Comment on the morphology of the red blood cells.
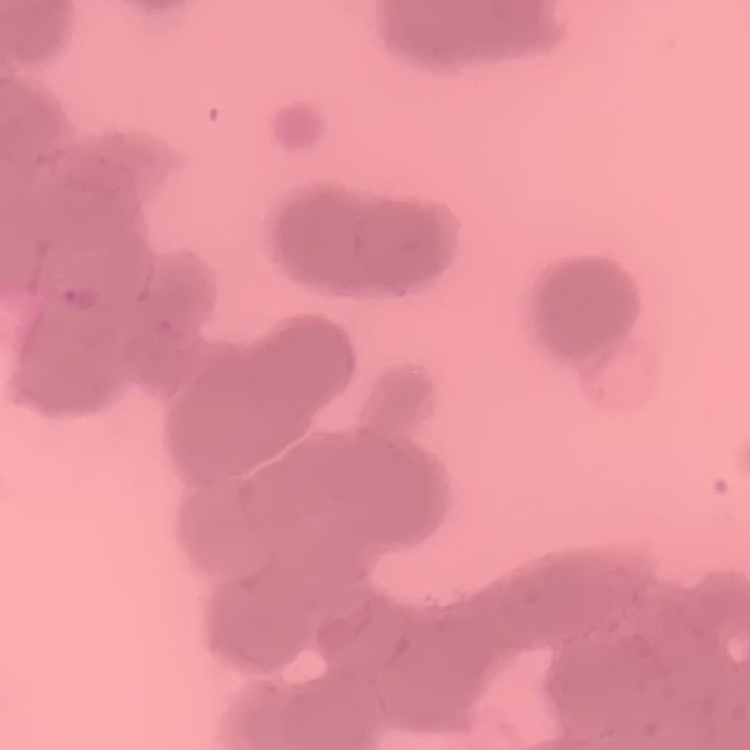

They show rouleaux formation.

Summary:
  - Stain: Field's or Giemsa
  - Preparation: thin blood smear
  - Image type: square crop of a larger photomicrograph